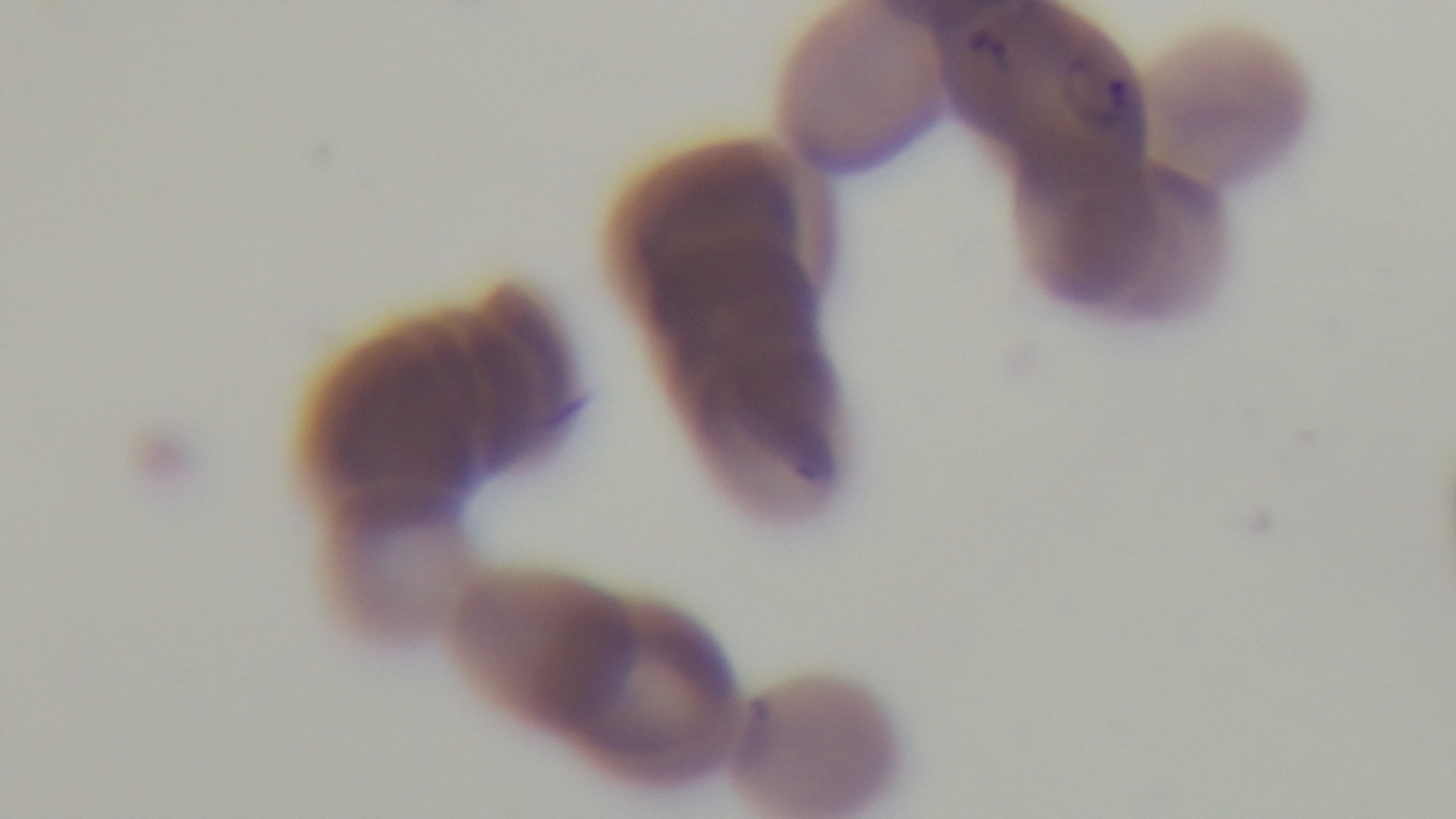

{
  "modality": "light microscopy",
  "stain": "Giemsa",
  "malaria_status": "positive",
  "field_of_view": "one from the slide",
  "capture": "mounted 4K digital camera",
  "objective": "100x oil immersion",
  "preparation": "thin blood film"
}